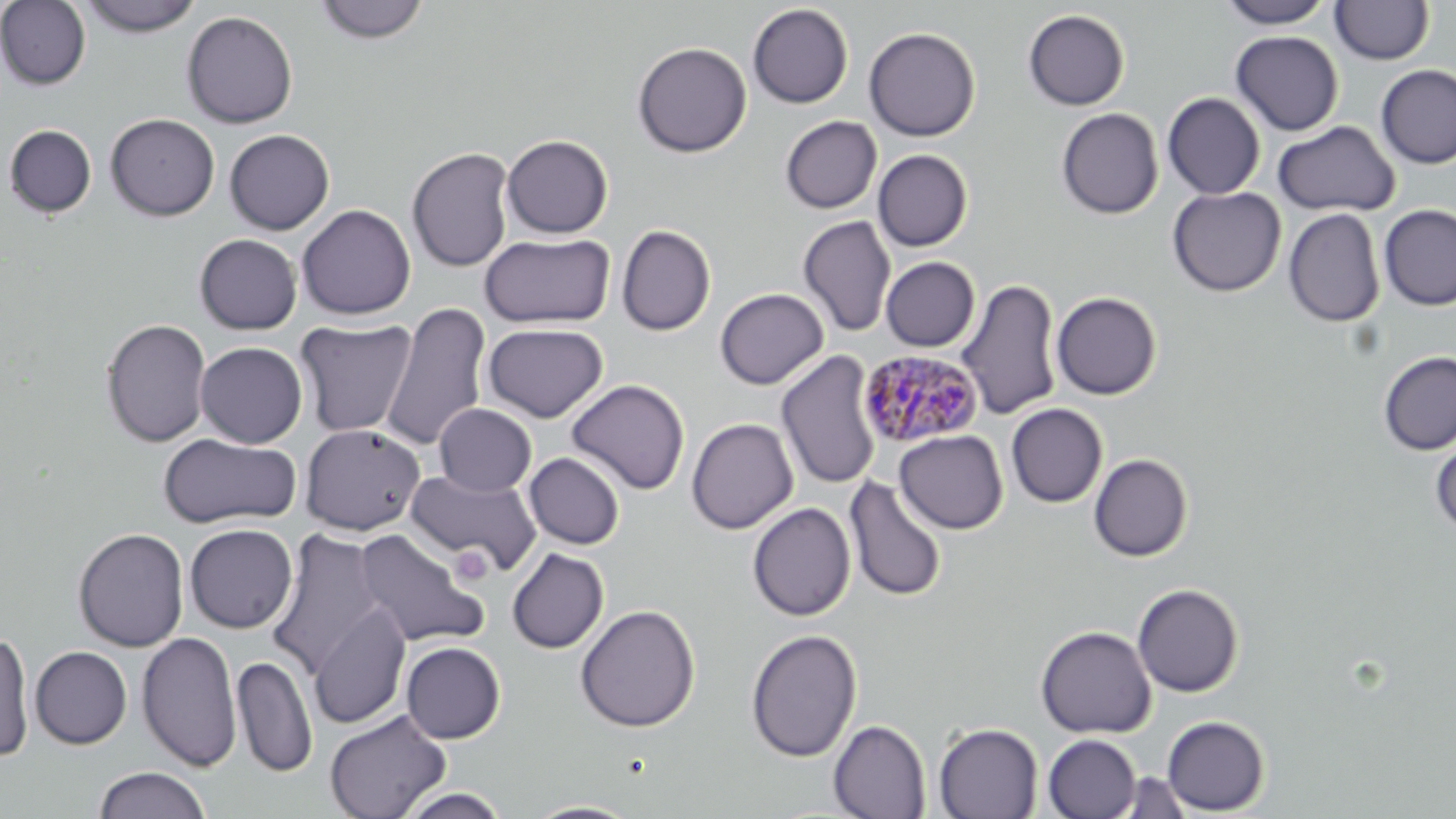
Approximate bounding boxes as [x1, y1, x2, y2] in pixels. Platelet locations: [450, 546, 494, 586]. Plasmodium malariae-infected red blood cell locations: [857, 348, 984, 449]. Uninfected red blood cell locations: [314, 0, 430, 44], [1217, 0, 1335, 28], [1330, 0, 1434, 64], [0, 1, 91, 90], [79, 1, 204, 36], [748, 4, 854, 108], [1023, 9, 1130, 110], [181, 10, 298, 128], [864, 26, 981, 141], [1230, 31, 1344, 136], [632, 41, 752, 158], [1375, 65, 1456, 169], [1162, 92, 1266, 200], [1056, 108, 1163, 219], [105, 113, 220, 221], [780, 116, 882, 213], [1272, 120, 1400, 217], [4, 124, 96, 217], [224, 129, 334, 235], [501, 134, 613, 238], [407, 146, 515, 273], [873, 149, 973, 251], [1167, 186, 1286, 297], [296, 204, 415, 320], [1378, 204, 1456, 311], [1284, 208, 1385, 328], [798, 215, 897, 338], [617, 225, 716, 335], [194, 233, 303, 335], [480, 233, 615, 328], [881, 257, 980, 352], [957, 278, 1062, 421], [715, 288, 829, 390], [1051, 291, 1162, 399], [381, 302, 492, 451], [295, 318, 418, 437], [101, 319, 211, 448], [482, 322, 609, 423], [195, 341, 308, 448], [776, 350, 882, 491], [1377, 350, 1456, 456], [566, 378, 690, 495], [434, 403, 536, 497], [1006, 403, 1107, 508], [687, 418, 798, 534], [300, 423, 426, 535], [894, 430, 1008, 534], [159, 432, 302, 529], [1430, 436, 1456, 536], [524, 453, 625, 549], [1088, 453, 1193, 562], [406, 469, 541, 575], [844, 475, 948, 601], [747, 502, 856, 621], [184, 523, 298, 634], [73, 527, 190, 652], [354, 528, 489, 649], [267, 529, 388, 679], [507, 548, 609, 653], [1132, 583, 1245, 697], [308, 604, 411, 730], [575, 604, 700, 732], [1035, 625, 1157, 738], [745, 628, 863, 762], [0, 630, 35, 762], [136, 631, 242, 772], [401, 641, 506, 744], [30, 646, 131, 749], [232, 655, 316, 777], [324, 709, 451, 819], [1162, 715, 1270, 815], [829, 719, 931, 819], [933, 722, 1043, 819], [1042, 734, 1142, 819], [94, 766, 211, 819], [1115, 772, 1196, 818], [395, 788, 512, 818], [522, 800, 643, 818]. Slide-level diagnosis: Plasmodium malariae. Thin blood smear. Image is 1456×819 pixels. Optical microscopy. 1000x magnification. Single field of view. May-Grünwald-Giemsa stain.